Look for Plasmodium parasites.
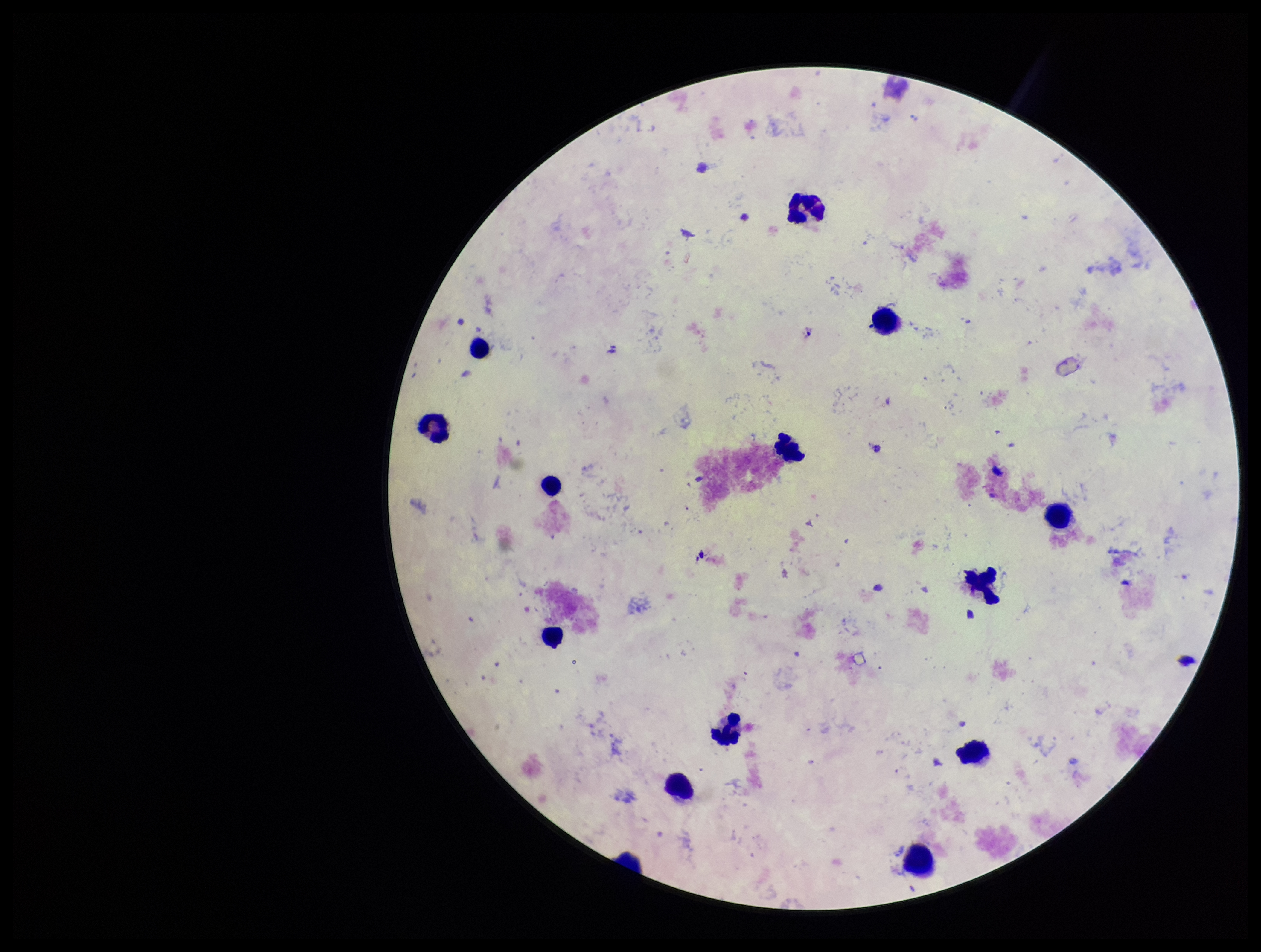

None seen.

Parasite count: 0. Preparation: thick blood smear. Giemsa stain. Image is 1261×952 pixels. One field from this slide. Photographed through the microscope eyepiece with a smartphone camera. Leukocyte count: 13. Patient malaria status: negative.